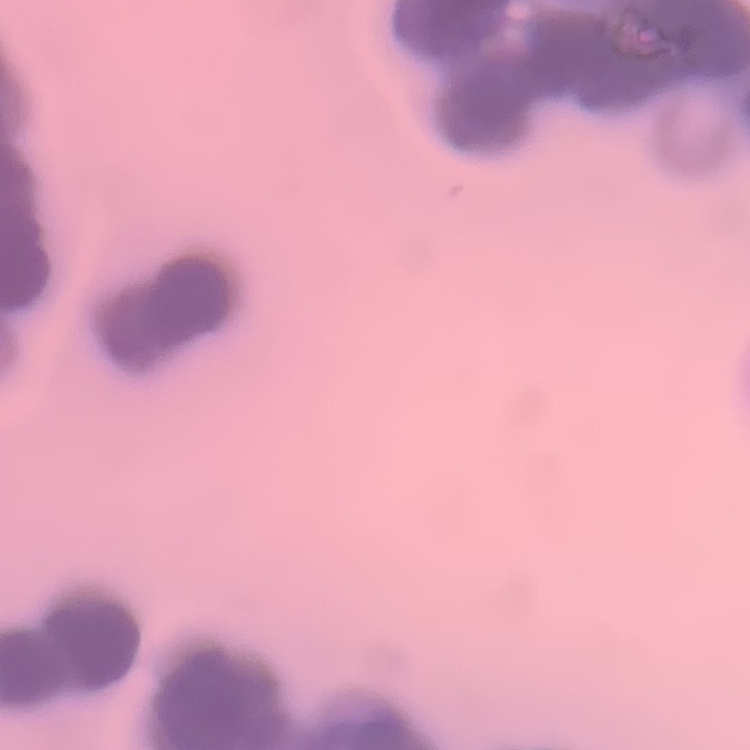

red_blood_cell_morphology: rouleaux formation
image_type: one tile cut from a larger photomicrograph
stain: Field's or Giemsa
preparation: thin blood smear